Assess this cell for malaria.
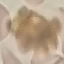

It is uninfected.

Thin blood smear. Cell patch, automatically extracted from a larger field of view and resized to 64 × 64 pixels. Giemsa stain. Acquired by smartphone through the microscope eyepiece.